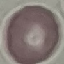

Malaria status: uninfected. Cell patch, automatically extracted from a larger field of view and resized to 64 × 64 pixels. Thin smear of blood. Acquired by smartphone through the microscope eyepiece. Giemsa stain.